Assess this cell for malaria.
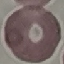

Uninfected.

Summary:
  - Preparation: thin blood film
  - Image type: cell patch, automatically extracted from a larger field of view and resized to 64 × 64 pixels
  - Stain: Giemsa
  - Capture: smartphone through the microscope eyepiece